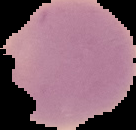
Image is 136×130 pixels. Segmented cell region on a black background. From a thin blood smear. Malaria status: uninfected.